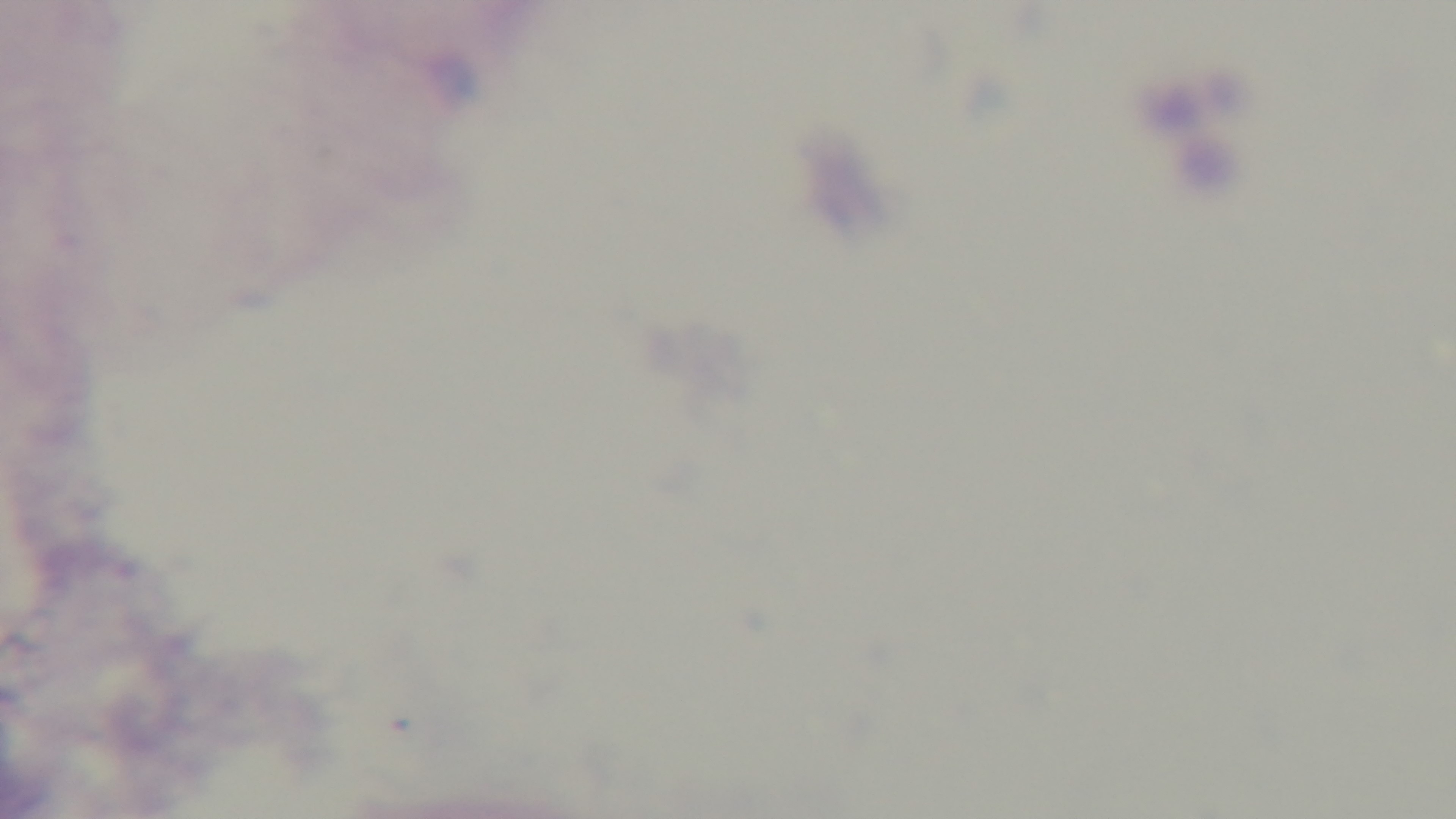

Summary:
  - Modality: light microscopy
  - Preparation: thick smear
  - Objective: 100x oil immersion
  - Field of view: single
  - Malaria status: negative
  - Stain: Giemsa
  - Capture: mounted 4K digital camera